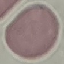
malaria status = uninfected
stain = Giemsa
preparation = thin blood smear
image type = automatically extracted cell patch, resized to 64 × 64 pixels
capture = smartphone camera at the microscope eyepiece